Locate every parasitized RBC.
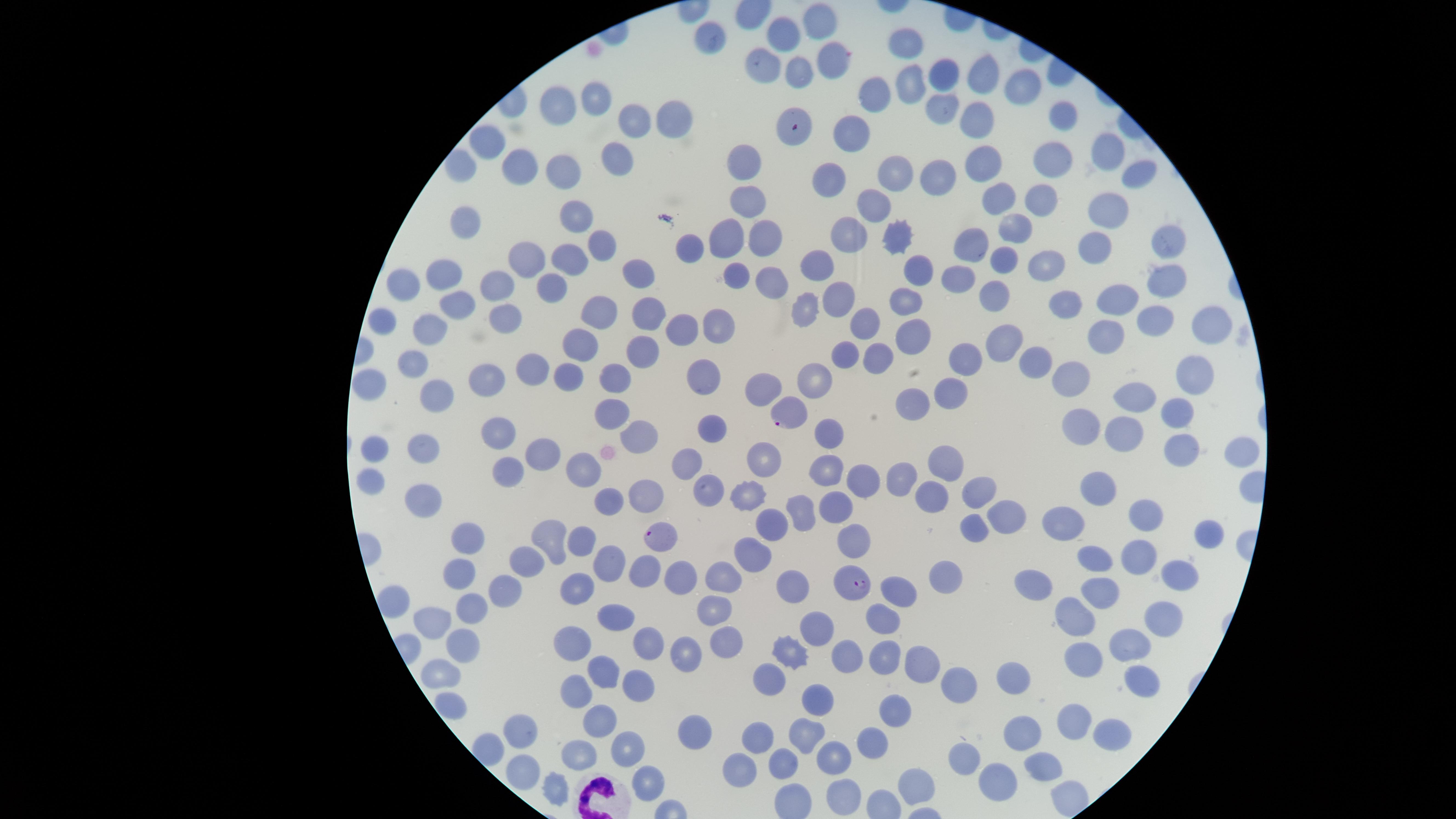

Approximate marker points, in pixels from the top-left corner.
Parasitized RBCs: (x=790, y=412), (x=666, y=535), (x=854, y=586).

Approximate marker points, in pixels from the top-left corner.
Summary:
  - WBCs: (x=601, y=800)
  - Uninfected RBCs: (x=819, y=18), (x=781, y=35), (x=707, y=39), (x=904, y=39), (x=831, y=60), (x=764, y=67), (x=979, y=73), (x=798, y=75), (x=942, y=77), (x=908, y=78), (x=1025, y=87), (x=593, y=97), (x=873, y=98), (x=944, y=98), (x=558, y=105), (x=1060, y=112), (x=982, y=118), (x=636, y=119), (x=674, y=120), (x=854, y=134), (x=1106, y=142), (x=482, y=143), (x=618, y=158), (x=985, y=158), (x=1060, y=162), (x=517, y=163), (x=744, y=163), (x=463, y=164), (x=562, y=166), (x=1146, y=172), (x=944, y=174), (x=900, y=175), (x=834, y=178), (x=999, y=197), (x=1039, y=198), (x=747, y=199), (x=880, y=203), (x=1105, y=209), (x=577, y=221), (x=467, y=223), (x=768, y=232), (x=845, y=234), (x=728, y=235), (x=1014, y=235), (x=896, y=237), (x=1166, y=238), (x=601, y=246), (x=690, y=246), (x=971, y=246), (x=1093, y=248), (x=528, y=255), (x=1048, y=256), (x=570, y=258), (x=1002, y=259), (x=817, y=265), (x=914, y=270), (x=736, y=273), (x=446, y=276), (x=636, y=276), (x=1166, y=276), (x=770, y=279), (x=963, y=280), (x=494, y=282), (x=554, y=282), (x=411, y=283), (x=995, y=297), (x=840, y=299), (x=1066, y=300), (x=1117, y=300), (x=901, y=301), (x=462, y=302), (x=799, y=310), (x=650, y=311), (x=600, y=315), (x=501, y=317), (x=1154, y=318), (x=380, y=319), (x=722, y=320), (x=863, y=322), (x=424, y=325), (x=1215, y=326), (x=685, y=328), (x=912, y=333), (x=581, y=340), (x=1003, y=341), (x=1107, y=341), (x=646, y=349), (x=839, y=355), (x=416, y=360), (x=882, y=360), (x=1033, y=364), (x=529, y=366), (x=964, y=366), (x=571, y=374), (x=1071, y=375), (x=481, y=377), (x=376, y=378), (x=706, y=378), (x=1189, y=378), (x=815, y=380), (x=617, y=381), (x=438, y=391), (x=764, y=391), (x=952, y=392), (x=1134, y=395), (x=911, y=405), (x=1176, y=409), (x=611, y=411), (x=715, y=427), (x=1083, y=427), (x=828, y=429), (x=1123, y=430), (x=492, y=431), (x=641, y=431), (x=1174, y=447), (x=373, y=449), (x=421, y=451), (x=547, y=452), (x=944, y=458), (x=767, y=461), (x=691, y=469), (x=583, y=470), (x=825, y=471), (x=507, y=472), (x=907, y=478), (x=373, y=481), (x=860, y=481), (x=1109, y=484), (x=710, y=487), (x=975, y=487), (x=753, y=492), (x=646, y=495), (x=937, y=495), (x=604, y=499), (x=427, y=501), (x=838, y=507), (x=800, y=511), (x=1004, y=513), (x=1148, y=514), (x=1068, y=518), (x=973, y=524), (x=772, y=526), (x=554, y=533), (x=1206, y=534), (x=857, y=535), (x=472, y=537), (x=584, y=540), (x=754, y=549), (x=527, y=553), (x=1139, y=553), (x=1096, y=557), (x=611, y=559), (x=674, y=570), (x=641, y=571), (x=946, y=573), (x=721, y=575), (x=461, y=576), (x=1179, y=582), (x=784, y=584), (x=1039, y=585), (x=1103, y=589), (x=896, y=590), (x=494, y=591), (x=580, y=592), (x=395, y=600), (x=720, y=607), (x=471, y=609), (x=612, y=614), (x=1162, y=614), (x=1071, y=617), (x=879, y=619), (x=432, y=622), (x=814, y=625), (x=467, y=640), (x=577, y=640), (x=1127, y=642), (x=725, y=644), (x=649, y=646), (x=684, y=650), (x=887, y=652), (x=787, y=654), (x=852, y=659), (x=922, y=659), (x=1082, y=659), (x=596, y=666), (x=767, y=672), (x=438, y=673), (x=1141, y=678), (x=635, y=681), (x=1018, y=681), (x=955, y=685), (x=576, y=686), (x=816, y=700), (x=451, y=701), (x=890, y=710), (x=1074, y=719), (x=602, y=720), (x=1115, y=727), (x=523, y=729), (x=696, y=730), (x=802, y=733), (x=1028, y=737), (x=757, y=738), (x=871, y=744), (x=488, y=747), (x=624, y=749), (x=580, y=753), (x=965, y=757), (x=833, y=760), (x=1041, y=762), (x=785, y=765), (x=741, y=766), (x=519, y=768), (x=993, y=776), (x=647, y=778), (x=916, y=780), (x=551, y=786), (x=842, y=790)
  - Visible region: circular
  - Image size: 1456×819 pixels
  - Species: Plasmodium falciparum
  - Field of view: single
  - Preparation: thin blood smear
  - Capture: smartphone photograph through the microscope eyepiece
  - Stain: Giemsa